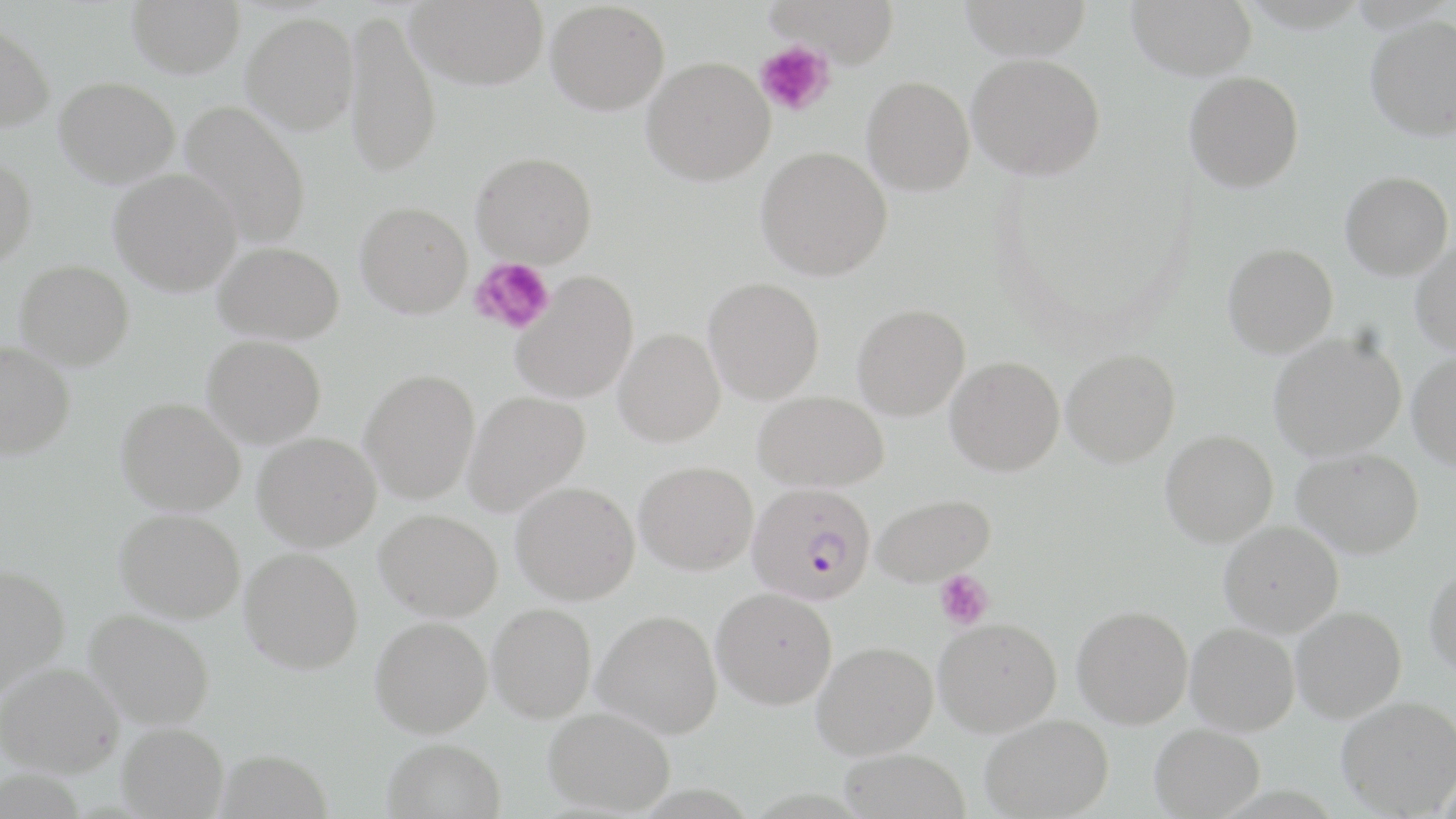 Approximate bounding boxes as [x1, y1, x2, y2] in pixels. Uninfected red blood cell locations (subset): [127, 0, 245, 77], [407, 0, 549, 89], [766, 0, 900, 64], [958, 0, 1094, 59], [1127, 0, 1257, 80], [546, 1, 670, 115], [344, 11, 442, 176], [242, 13, 359, 134], [1366, 15, 1456, 140], [0, 22, 56, 132], [967, 54, 1105, 180], [642, 56, 775, 185], [1184, 70, 1305, 192], [861, 75, 974, 195], [54, 76, 180, 187], [179, 100, 312, 248], [756, 146, 892, 280], [471, 151, 597, 267], [0, 156, 37, 269], [109, 169, 242, 296], [1341, 171, 1453, 280], [355, 201, 473, 318], [1410, 239, 1456, 356], [214, 241, 345, 344], [1223, 243, 1338, 357], [14, 259, 134, 370], [511, 271, 639, 403], [703, 277, 825, 404], [852, 304, 970, 420], [613, 328, 724, 446], [1268, 332, 1406, 461], [202, 335, 326, 447], [0, 342, 75, 460], [1062, 349, 1181, 466], [1408, 352, 1456, 470], [945, 356, 1064, 476], [360, 369, 480, 503], [463, 390, 590, 515], [754, 391, 888, 492], [117, 397, 245, 516], [1160, 430, 1278, 546], [253, 432, 381, 551], [1293, 448, 1424, 557], [635, 461, 758, 574], [511, 481, 639, 604], [872, 493, 995, 586], [114, 508, 245, 623], [374, 509, 503, 621], [1219, 521, 1343, 637], [240, 547, 363, 674], [0, 564, 70, 699], [1426, 565, 1456, 676], [712, 587, 837, 709], [488, 603, 596, 722], [1073, 605, 1193, 728], [1291, 606, 1406, 722], [85, 609, 215, 729], [592, 609, 723, 737], [370, 616, 492, 737], [934, 617, 1062, 737], [1186, 622, 1300, 735], [812, 641, 938, 759], [0, 661, 124, 777], [1337, 695, 1456, 816], [544, 706, 675, 816], [980, 714, 1114, 818], [117, 722, 229, 818], [1150, 723, 1265, 818], [382, 738, 506, 819], [838, 747, 970, 819]. Platelet locations (subset): [470, 258, 555, 334], [934, 570, 994, 630]. Plasmodium falciparum-infected red blood cell locations: [748, 482, 876, 605]. Slide-level diagnosis: Plasmodium falciparum. Optical microscopy. Thin blood film. One field of a larger specimen. 1000x magnification. May-Grünwald-Giemsa-stained preparation. Image is 1456×819 pixels.